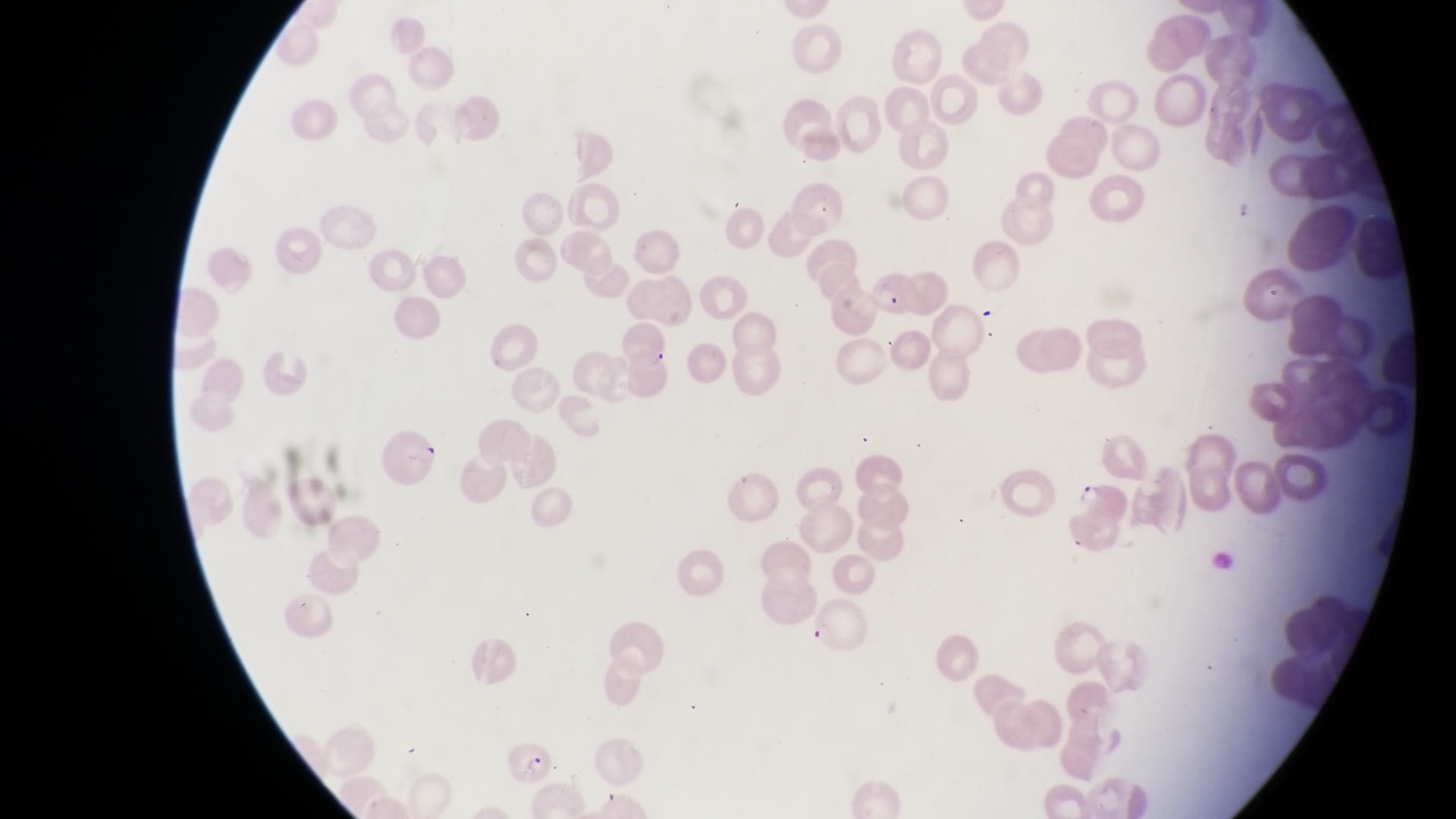

magnification: 1000x
image_size: 1456×819 pixels
field_of_view: single
preparation: thin blood film
parasitised_red_blood_cell_locations: 'approximate bounding boxes as left top right bottom in pixels: 871 271 916 314; 618 325 674 377; 383 428 446 491; 806 594 875 655; 502 746 551 785'
capture: smartphone photograph through the eyepiece of an Olympus CX-23 microscope
country: Uganda
trophozoite_locations: 'approximate bounding boxes as left top right bottom in pixels: 1073 478 1107 507'